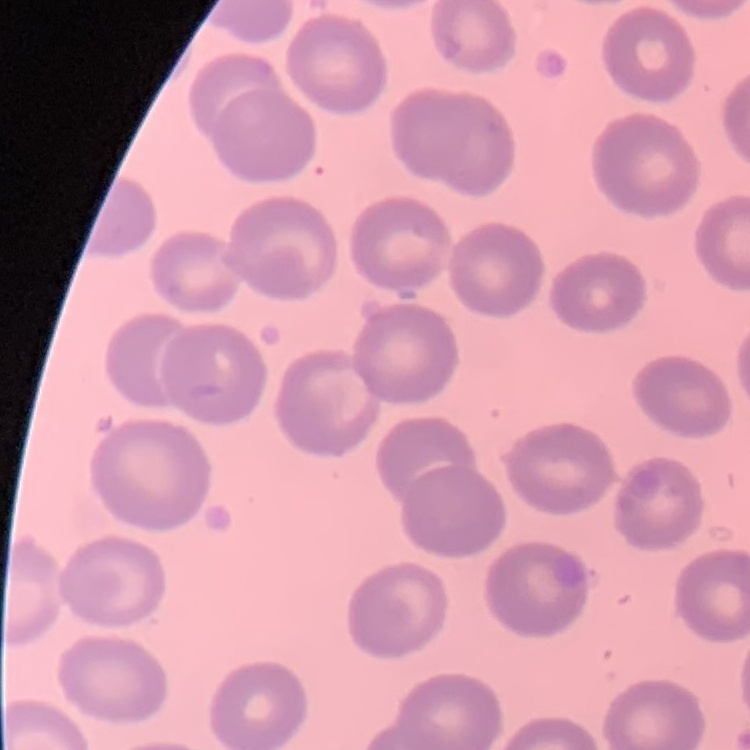

Summary:
  - Erythrocyte morphology: no rouleaux formation
  - Preparation: thin blood film
  - Image type: square crop of a larger photomicrograph
  - Stain: Field's or Giemsa